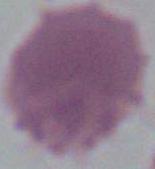
Summary:
  - Identification: red blood cell
  - Modality: micrograph
  - Magnification: 1000x